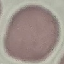 Result: negative for malaria parasites. Acquired by smartphone through the microscope eyepiece. Giemsa-stained preparation. Cell patch, automatically extracted from a larger field of view and resized to 64 × 64 pixels. Thin blood film.